Mark where platelets are.
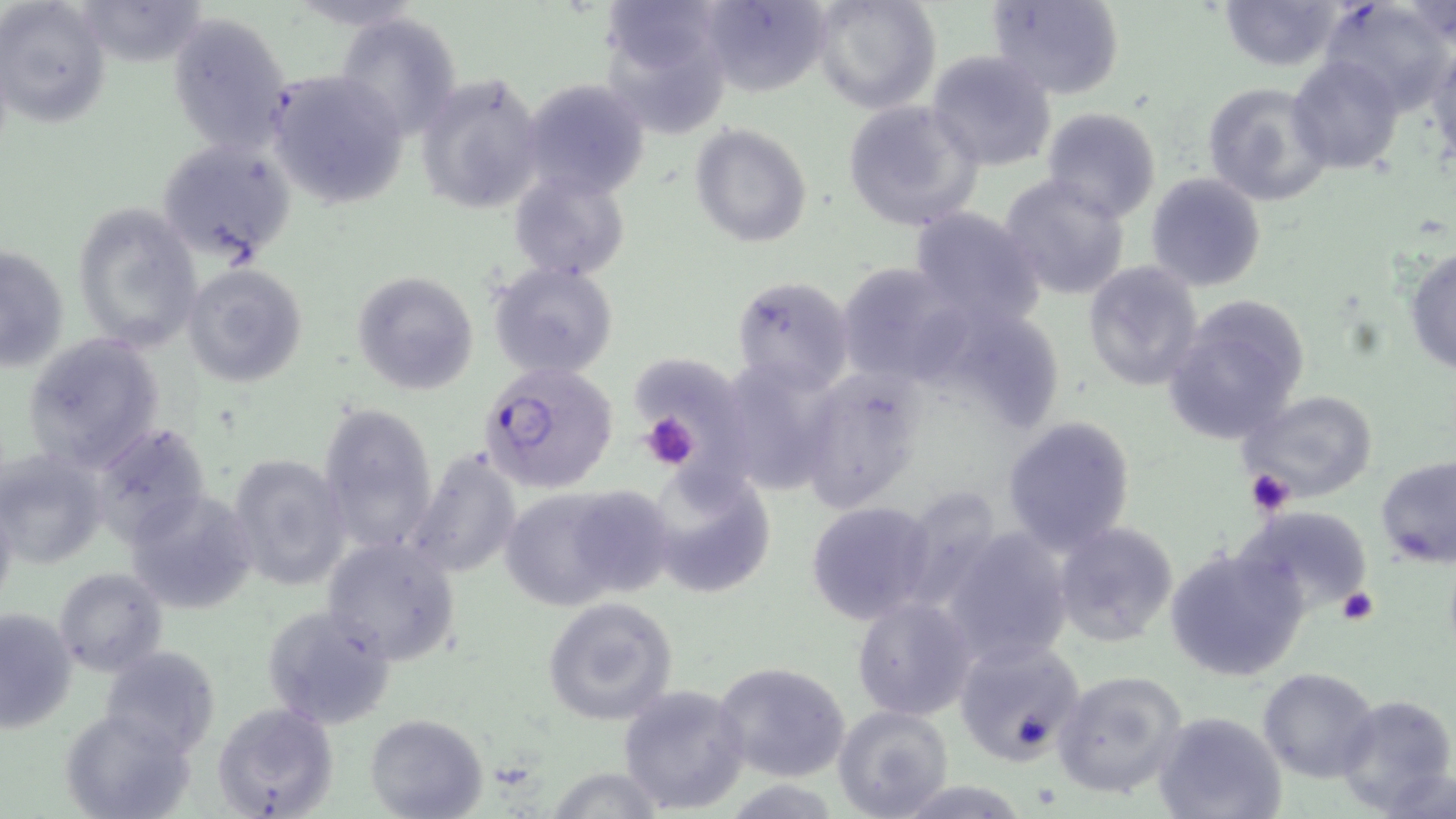
Approximate bounding boxes as (x1, y1, x2, y2) in pixels.
Platelets: (637, 410, 701, 471), (1245, 469, 1296, 517), (1337, 585, 1380, 627).

Summary:
  - Uninfected red blood cell locations: (695, 0, 834, 99), (811, 0, 940, 115), (986, 0, 1127, 100), (1218, 0, 1344, 73), (1, 1, 110, 127), (1320, 1, 1452, 110), (595, 2, 735, 127), (1400, 2, 1455, 46), (168, 11, 294, 153), (333, 11, 465, 140), (1428, 40, 1456, 167), (926, 49, 1058, 172), (1288, 55, 1405, 174), (267, 69, 409, 209), (415, 71, 548, 213), (519, 76, 653, 200), (1202, 80, 1331, 205), (842, 99, 985, 232), (1040, 105, 1161, 222), (690, 124, 812, 247), (156, 137, 295, 264), (510, 172, 631, 280), (999, 173, 1133, 302), (1144, 173, 1268, 292), (70, 202, 202, 352), (906, 207, 1049, 329), (0, 241, 70, 376), (1404, 244, 1456, 377), (1081, 260, 1204, 391), (489, 262, 620, 382), (832, 262, 969, 384), (180, 263, 308, 388), (351, 271, 478, 395), (731, 276, 855, 396), (1164, 295, 1312, 444), (22, 331, 167, 470), (633, 362, 756, 508), (733, 362, 835, 492), (800, 370, 924, 511), (1239, 388, 1381, 502), (317, 401, 438, 553), (1001, 415, 1137, 554), (93, 425, 214, 543), (406, 446, 523, 580), (0, 448, 108, 569), (226, 454, 351, 593), (1375, 455, 1455, 569), (644, 463, 775, 598), (496, 483, 671, 612), (0, 487, 19, 613), (902, 488, 995, 609), (125, 489, 260, 614), (804, 501, 937, 626), (1237, 503, 1373, 616), (1051, 521, 1179, 646), (938, 527, 1076, 670), (320, 536, 462, 666), (1164, 544, 1311, 683), (54, 567, 168, 677), (541, 596, 678, 726), (850, 596, 977, 721), (260, 605, 398, 730), (0, 606, 79, 734), (953, 635, 1086, 765), (99, 646, 221, 754), (714, 662, 852, 784), (1258, 667, 1379, 782), (1052, 668, 1189, 800), (616, 684, 750, 814), (1334, 693, 1455, 817), (212, 703, 339, 819), (833, 704, 955, 819), (61, 707, 196, 819), (1153, 711, 1286, 819), (364, 713, 486, 819), (544, 767, 665, 818), (888, 779, 1033, 816)
  - Plasmodium falciparum-infected red blood cell locations: (480, 362, 620, 492)
  - Slide-level diagnosis: Plasmodium falciparum
  - Preparation: thin blood film
  - Stain: May-Grünwald-Giemsa
  - Image size: 1456×819 pixels
  - Field of view: single
  - Magnification: 1000x
  - Modality: optical microscopy